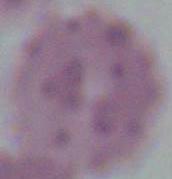

magnification = 1000x
modality = micrograph
identification = erythrocyte